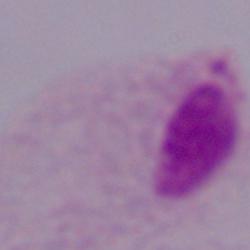 A trichomonad is shown. 1000x magnification. Micrograph.